Describe the morphology of the erythrocytes.
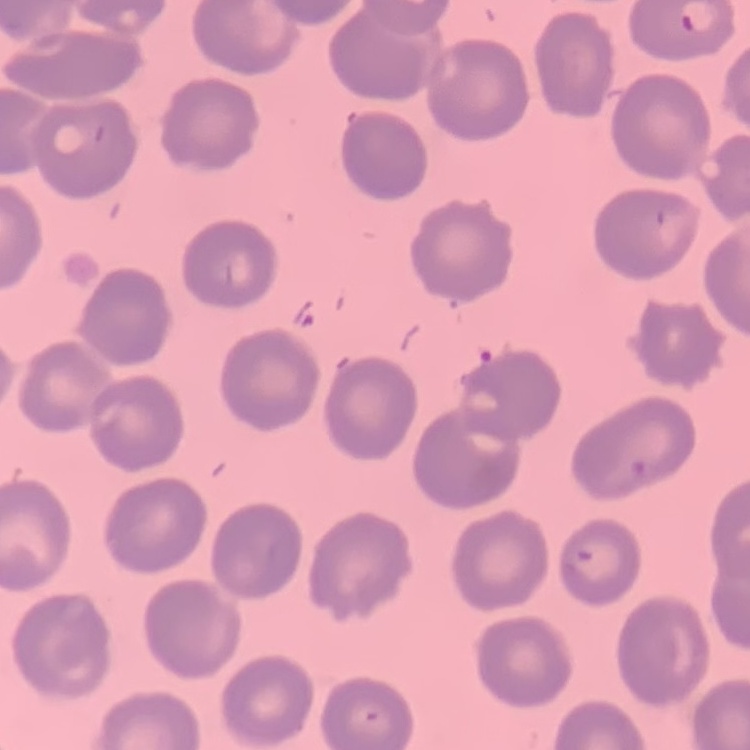

They show no rouleaux formation.

Summary:
  - Stain: Field's or Giemsa
  - Image type: one tile cut from a larger photomicrograph
  - Preparation: thin blood smear